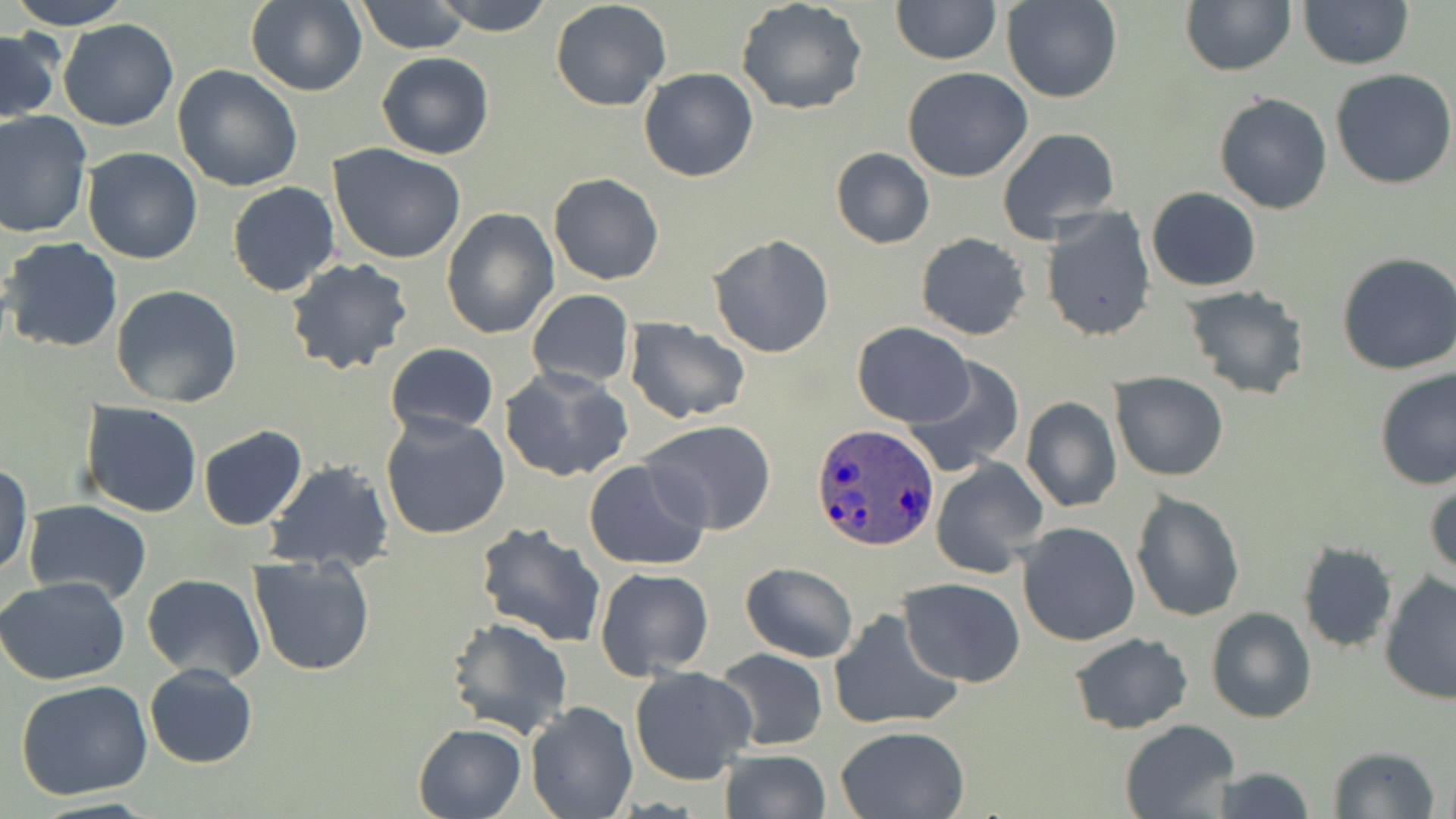
Approximate bounding boxes as (x1, y1, x2, y2) in pixels. Uninfected red blood cell locations: (10, 0, 133, 29), (357, 0, 472, 54), (433, 0, 554, 35), (891, 0, 1001, 65), (1003, 0, 1122, 103), (1180, 0, 1296, 75), (245, 1, 367, 97), (551, 1, 672, 112), (736, 1, 868, 116), (1298, 1, 1413, 70), (59, 18, 178, 131), (1, 28, 60, 125), (375, 51, 494, 159), (173, 63, 304, 191), (639, 67, 759, 182), (903, 67, 1033, 181), (1329, 67, 1456, 190), (1214, 91, 1334, 214), (0, 111, 94, 239), (995, 126, 1122, 243), (328, 144, 469, 264), (80, 147, 203, 264), (831, 147, 933, 248), (259, 163, 449, 287), (548, 172, 664, 285), (227, 181, 340, 296), (1146, 187, 1262, 292), (1040, 206, 1155, 343), (440, 209, 558, 339), (915, 232, 1032, 340), (708, 234, 836, 357), (1, 237, 123, 353), (1337, 250, 1456, 376), (285, 257, 411, 375), (110, 285, 243, 407), (1182, 286, 1312, 400), (527, 289, 634, 390), (624, 318, 750, 424), (852, 323, 974, 427), (385, 343, 500, 438), (902, 358, 1025, 479), (501, 366, 633, 483), (1375, 366, 1456, 490), (1112, 373, 1227, 481), (1020, 396, 1122, 512), (78, 401, 203, 520), (380, 412, 510, 540), (640, 419, 780, 535), (197, 425, 308, 531), (929, 458, 1047, 578), (584, 459, 710, 569), (264, 460, 395, 573), (0, 462, 33, 580), (1426, 472, 1456, 582), (1129, 489, 1246, 623), (22, 500, 151, 603), (473, 520, 607, 647), (1016, 521, 1142, 647), (1296, 542, 1398, 655), (248, 554, 378, 677), (741, 562, 858, 663), (594, 567, 714, 679), (141, 573, 266, 683), (1379, 573, 1456, 704), (0, 577, 130, 687), (900, 577, 1025, 686), (1205, 607, 1317, 725), (829, 608, 963, 732), (445, 616, 574, 740), (1069, 631, 1193, 735), (714, 648, 829, 750), (144, 663, 258, 769), (629, 665, 758, 786), (15, 680, 155, 803), (525, 701, 638, 818), (1119, 720, 1240, 818), (412, 723, 526, 819), (834, 725, 969, 818), (1327, 746, 1441, 819), (717, 749, 832, 819), (1205, 767, 1316, 819). Plasmodium ovale-infected red blood cell locations: (812, 421, 939, 551). Slide-level diagnosis: Plasmodium ovale. May-Grünwald-Giemsa stain. Light microscopy. Captured at 1000x magnification. One field of a larger specimen. Thin blood film. Image is 1456×819 pixels.